Identify the parasite.
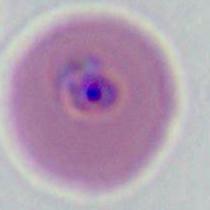
This is Plasmodium.

Summary:
  - Magnification: 400x or 1000x
  - Modality: micrograph